Name the parasite shown.
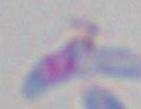
This is Toxoplasma gondii.

Micrograph. Captured at 1000x magnification.